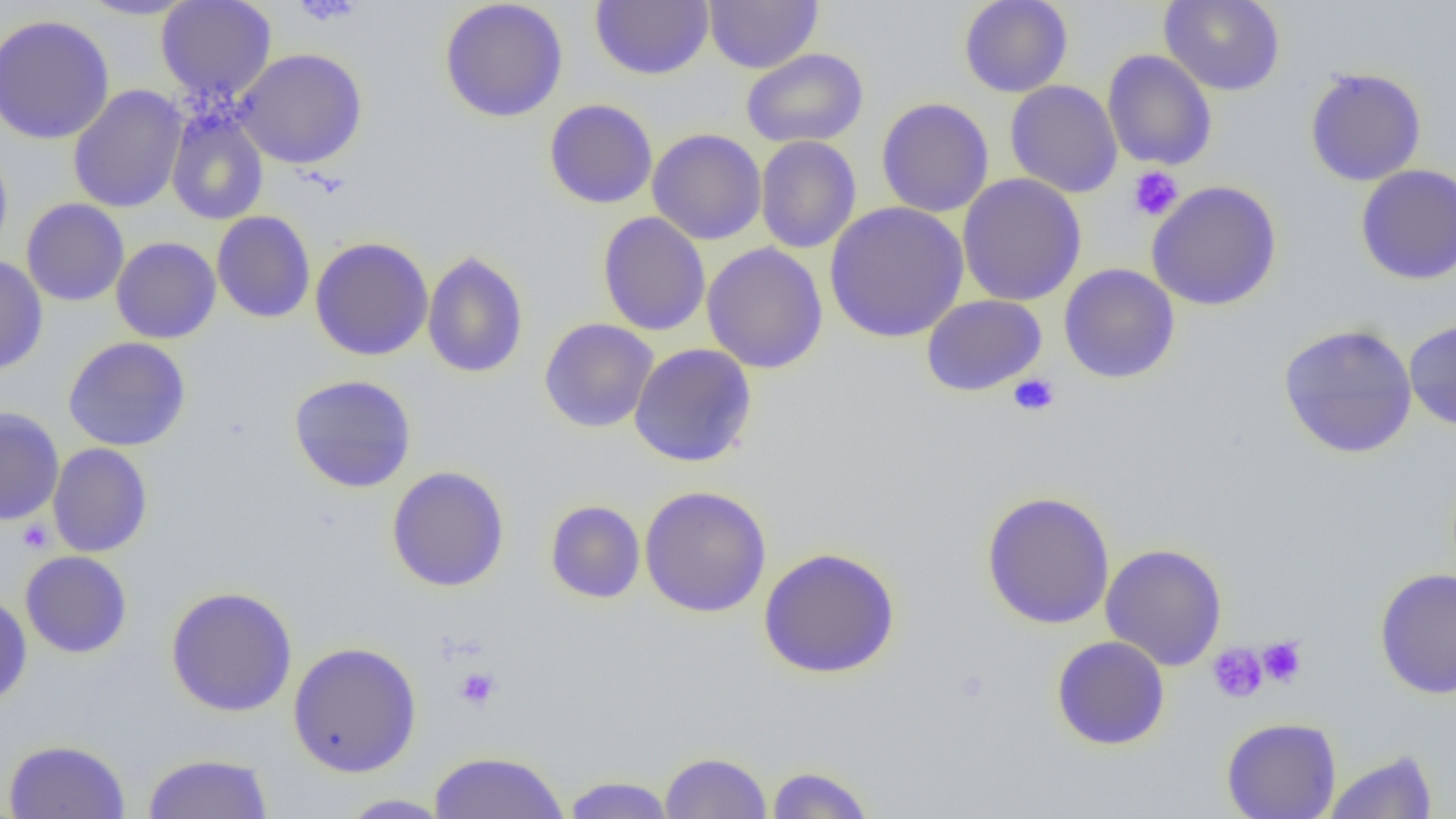
slide-level diagnosis = no evidence of blood parasites
image size = 1456×819 pixels
magnification = 1000x
preparation = thin blood film
uninfected red blood cell locations = approximate bounding boxes as (x1,y1)-(x2,y2) corner pairs in pixels: (76,0)-(199,20), (591,0)-(714,80), (704,0)-(823,73), (958,0)-(1073,98), (1158,0)-(1286,96), (155,1)-(276,101), (438,1)-(568,122), (0,14)-(115,144), (233,48)-(368,169), (740,48)-(868,148), (1102,49)-(1217,171), (1304,67)-(1427,186), (1005,80)-(1123,198), (67,85)-(187,213), (876,97)-(994,218), (544,98)-(658,210), (166,107)-(269,225), (647,129)-(767,245), (755,135)-(861,254), (0,144)-(13,261), (1356,164)-(1456,285), (957,174)-(1087,306), (1146,180)-(1283,311), (21,199)-(130,306), (824,202)-(969,343), (212,210)-(316,323), (597,212)-(710,336), (110,236)-(221,344), (310,236)-(434,361), (701,242)-(829,374), (422,250)-(529,379), (0,254)-(48,374), (1059,263)-(1180,384), (921,294)-(1047,397), (539,318)-(659,433), (1404,318)-(1456,432), (1278,323)-(1418,459), (63,336)-(191,452), (629,343)-(758,468), (288,374)-(417,493), (0,407)-(64,525), (48,443)-(153,558), (386,465)-(510,592), (639,485)-(772,618), (980,490)-(1116,630), (545,500)-(646,603), (1100,543)-(1228,670), (758,546)-(901,679), (20,550)-(132,658), (1375,567)-(1456,699), (166,586)-(298,717), (0,592)-(32,707), (1051,635)-(1171,751), (287,641)-(422,777), (1222,716)-(1341,819), (3,739)-(131,819), (1322,749)-(1438,818), (428,751)-(569,818), (659,751)-(772,818), (142,752)-(274,818), (764,765)-(875,818), (561,775)-(678,818), (336,794)-(452,818)
field of view = one of a larger specimen
modality = optical microscopy
platelet locations = approximate bounding boxes as (x1,y1)-(x2,y2) corner pairs in pixels: (290,0)-(365,25), (1127,166)-(1184,222), (1008,373)-(1060,417), (17,520)-(53,553), (1257,636)-(1306,688), (1207,643)-(1268,704), (454,667)-(501,711)